Classify this cell by malaria status.
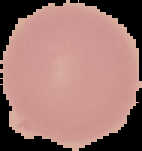
It is uninfected.

From a thin blood smear. Image is 142×151 pixels. The area outside the segmented cell region is set to black.